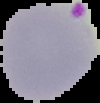

Summary:
  - Image size: 100×103 pixels
  - Preparation: thin blood film
  - Result: Plasmodium parasites identified
  - Image type: segmented cell region with the area outside set to black